Outline each blood parasite and name the species.
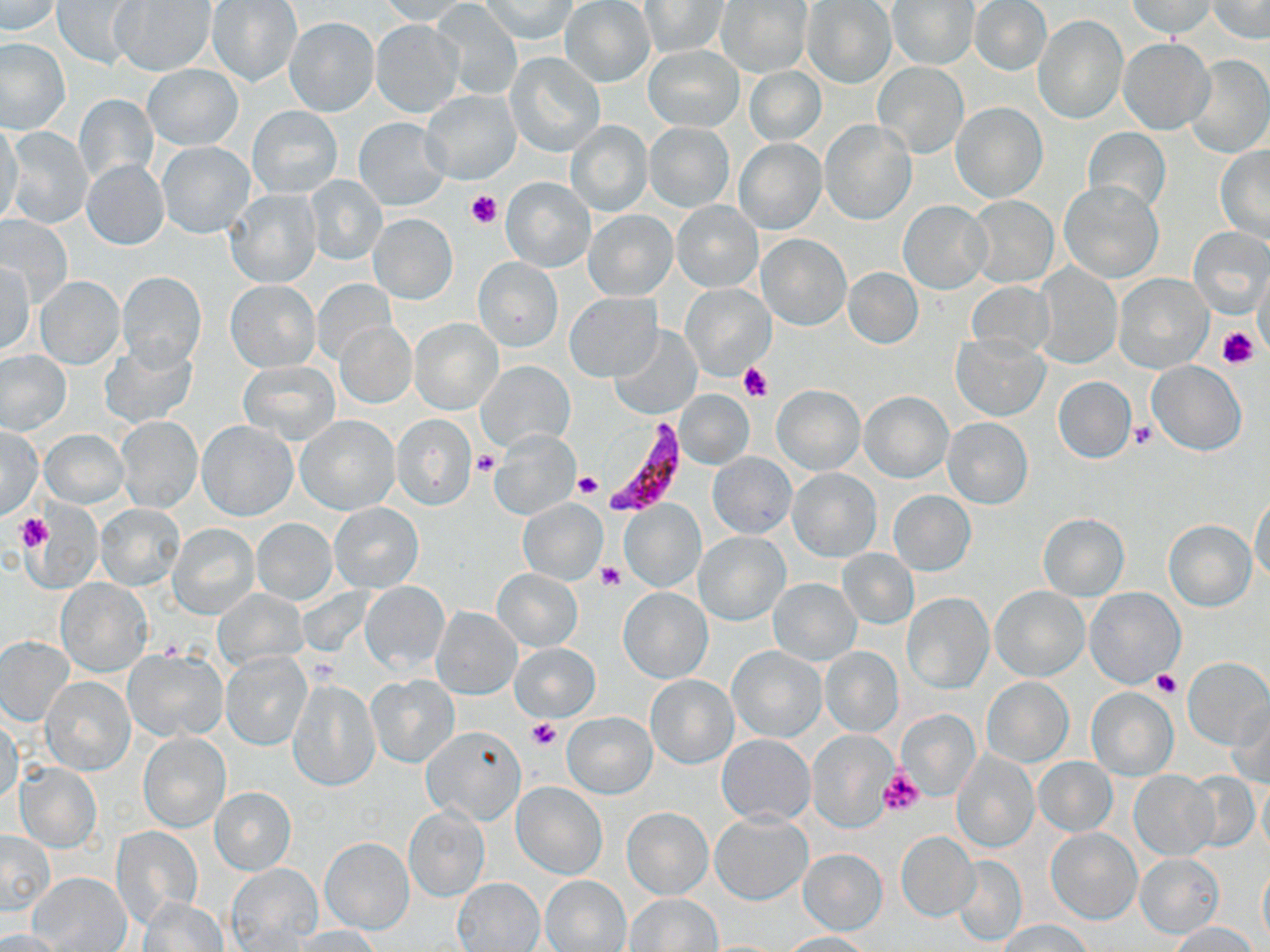

Approximate bounding boxes as named x1/y1/x2/y2 corners in pixels.
Plasmodium falciparum-infected red blood cells: (x1=599, y1=419, x2=692, y2=516).
No Plasmodium ovale, Plasmodium malariae, Plasmodium vivax, Babesia divergens, or Trypanosoma brucei observed.

Summary:
  - Uninfected red blood cell locations: (x1=53, y1=0, x2=140, y2=69), (x1=377, y1=0, x2=474, y2=26), (x1=560, y1=0, x2=655, y2=88), (x1=970, y1=0, x2=1051, y2=76), (x1=1129, y1=0, x2=1214, y2=38), (x1=1206, y1=0, x2=1270, y2=42), (x1=1, y1=1, x2=63, y2=35), (x1=110, y1=1, x2=216, y2=76), (x1=206, y1=1, x2=301, y2=86), (x1=481, y1=1, x2=577, y2=41), (x1=641, y1=1, x2=727, y2=57), (x1=890, y1=1, x2=977, y2=68), (x1=716, y1=2, x2=811, y2=78), (x1=802, y1=2, x2=895, y2=89), (x1=432, y1=4, x2=523, y2=98), (x1=1034, y1=15, x2=1127, y2=123), (x1=285, y1=16, x2=378, y2=117), (x1=370, y1=20, x2=464, y2=118), (x1=1, y1=38, x2=69, y2=133), (x1=1119, y1=38, x2=1213, y2=134), (x1=643, y1=45, x2=743, y2=132), (x1=506, y1=52, x2=604, y2=158), (x1=1186, y1=54, x2=1269, y2=157), (x1=873, y1=62, x2=969, y2=159), (x1=143, y1=64, x2=243, y2=150), (x1=744, y1=66, x2=825, y2=146), (x1=422, y1=89, x2=521, y2=184), (x1=73, y1=94, x2=158, y2=184), (x1=951, y1=103, x2=1048, y2=203), (x1=249, y1=105, x2=342, y2=198), (x1=353, y1=117, x2=449, y2=210), (x1=819, y1=119, x2=915, y2=223), (x1=564, y1=120, x2=652, y2=217), (x1=0, y1=121, x2=24, y2=226), (x1=644, y1=122, x2=734, y2=211), (x1=4, y1=127, x2=92, y2=229), (x1=1083, y1=127, x2=1171, y2=215), (x1=735, y1=139, x2=826, y2=234), (x1=158, y1=141, x2=255, y2=237), (x1=1215, y1=147, x2=1270, y2=242), (x1=82, y1=160, x2=168, y2=249), (x1=306, y1=176, x2=386, y2=263), (x1=500, y1=177, x2=596, y2=272), (x1=1059, y1=181, x2=1163, y2=283), (x1=225, y1=190, x2=320, y2=288), (x1=967, y1=196, x2=1058, y2=287), (x1=674, y1=199, x2=763, y2=293), (x1=899, y1=201, x2=990, y2=293), (x1=582, y1=209, x2=678, y2=301), (x1=368, y1=213, x2=457, y2=304), (x1=0, y1=215, x2=72, y2=307), (x1=1187, y1=227, x2=1269, y2=314), (x1=757, y1=234, x2=850, y2=330), (x1=472, y1=257, x2=563, y2=352), (x1=0, y1=259, x2=36, y2=354), (x1=1034, y1=263, x2=1122, y2=368), (x1=1254, y1=265, x2=1269, y2=360), (x1=844, y1=267, x2=923, y2=348), (x1=117, y1=272, x2=207, y2=369), (x1=1114, y1=273, x2=1212, y2=373), (x1=34, y1=275, x2=125, y2=369), (x1=226, y1=280, x2=319, y2=372), (x1=313, y1=280, x2=396, y2=365), (x1=965, y1=281, x2=1057, y2=358), (x1=682, y1=284, x2=774, y2=378), (x1=564, y1=292, x2=662, y2=381), (x1=409, y1=318, x2=502, y2=414), (x1=336, y1=320, x2=416, y2=408), (x1=610, y1=325, x2=703, y2=419), (x1=952, y1=335, x2=1048, y2=421), (x1=99, y1=341, x2=198, y2=428), (x1=1, y1=350, x2=71, y2=434), (x1=239, y1=360, x2=340, y2=444), (x1=478, y1=360, x2=575, y2=450), (x1=1147, y1=360, x2=1246, y2=455), (x1=1052, y1=375, x2=1136, y2=463), (x1=771, y1=385, x2=866, y2=475), (x1=676, y1=389, x2=753, y2=468), (x1=860, y1=390, x2=953, y2=483), (x1=295, y1=414, x2=399, y2=514), (x1=391, y1=414, x2=477, y2=510), (x1=115, y1=415, x2=202, y2=513), (x1=943, y1=417, x2=1033, y2=509), (x1=198, y1=420, x2=296, y2=521), (x1=1, y1=425, x2=40, y2=519), (x1=41, y1=428, x2=129, y2=507), (x1=489, y1=429, x2=580, y2=520), (x1=708, y1=453, x2=797, y2=538), (x1=787, y1=467, x2=881, y2=562), (x1=889, y1=491, x2=975, y2=575), (x1=1251, y1=491, x2=1270, y2=584), (x1=517, y1=498, x2=608, y2=585), (x1=620, y1=498, x2=706, y2=593), (x1=328, y1=501, x2=424, y2=592), (x1=96, y1=502, x2=187, y2=592), (x1=21, y1=506, x2=104, y2=593), (x1=1037, y1=514, x2=1129, y2=600), (x1=253, y1=518, x2=336, y2=605), (x1=1164, y1=519, x2=1256, y2=611), (x1=168, y1=524, x2=260, y2=620), (x1=695, y1=532, x2=788, y2=625), (x1=837, y1=548, x2=918, y2=629), (x1=492, y1=568, x2=582, y2=652), (x1=769, y1=578, x2=862, y2=666), (x1=57, y1=579, x2=150, y2=675), (x1=360, y1=581, x2=449, y2=674), (x1=990, y1=585, x2=1090, y2=681), (x1=618, y1=586, x2=712, y2=683), (x1=214, y1=589, x2=306, y2=668), (x1=1086, y1=589, x2=1187, y2=690), (x1=902, y1=593, x2=993, y2=693), (x1=431, y1=607, x2=522, y2=699), (x1=0, y1=637, x2=73, y2=725), (x1=511, y1=643, x2=600, y2=722), (x1=727, y1=645, x2=827, y2=742), (x1=821, y1=646, x2=902, y2=736), (x1=123, y1=650, x2=228, y2=742), (x1=222, y1=652, x2=310, y2=749), (x1=1182, y1=657, x2=1270, y2=749), (x1=365, y1=673, x2=460, y2=768), (x1=646, y1=674, x2=737, y2=768), (x1=41, y1=676, x2=135, y2=775), (x1=982, y1=676, x2=1073, y2=766), (x1=288, y1=677, x2=382, y2=791), (x1=1087, y1=687, x2=1178, y2=780), (x1=1229, y1=700, x2=1270, y2=787), (x1=897, y1=708, x2=981, y2=802), (x1=563, y1=711, x2=656, y2=798), (x1=0, y1=716, x2=22, y2=809), (x1=420, y1=725, x2=526, y2=824), (x1=805, y1=730, x2=897, y2=832), (x1=138, y1=732, x2=231, y2=832), (x1=718, y1=735, x2=814, y2=826), (x1=951, y1=750, x2=1038, y2=853), (x1=1034, y1=757, x2=1117, y2=836), (x1=15, y1=763, x2=102, y2=852), (x1=1129, y1=770, x2=1219, y2=860), (x1=1184, y1=771, x2=1261, y2=853), (x1=1257, y1=777, x2=1270, y2=859), (x1=513, y1=782, x2=606, y2=879), (x1=209, y1=786, x2=296, y2=875), (x1=622, y1=807, x2=713, y2=899), (x1=404, y1=808, x2=489, y2=901), (x1=712, y1=812, x2=812, y2=904), (x1=112, y1=826, x2=203, y2=925), (x1=1047, y1=828, x2=1141, y2=924), (x1=1, y1=830, x2=54, y2=914), (x1=897, y1=831, x2=979, y2=921), (x1=321, y1=837, x2=414, y2=934), (x1=799, y1=849, x2=887, y2=934), (x1=1135, y1=853, x2=1223, y2=937), (x1=951, y1=854, x2=1027, y2=945), (x1=227, y1=863, x2=322, y2=950), (x1=1258, y1=863, x2=1270, y2=946), (x1=31, y1=872, x2=131, y2=952), (x1=540, y1=874, x2=631, y2=952), (x1=454, y1=878, x2=545, y2=950), (x1=625, y1=893, x2=722, y2=951), (x1=139, y1=899, x2=227, y2=952), (x1=1000, y1=919, x2=1091, y2=952), (x1=1170, y1=921, x2=1260, y2=951), (x1=292, y1=926, x2=384, y2=951), (x1=0, y1=928, x2=69, y2=952), (x1=780, y1=932, x2=874, y2=952)
  - Platelet locations: (x1=467, y1=190, x2=503, y2=228), (x1=1217, y1=326, x2=1258, y2=367), (x1=740, y1=362, x2=772, y2=400), (x1=1130, y1=421, x2=1157, y2=449), (x1=474, y1=451, x2=501, y2=477), (x1=571, y1=473, x2=601, y2=498), (x1=16, y1=512, x2=71, y2=570), (x1=17, y1=514, x2=52, y2=552), (x1=597, y1=561, x2=626, y2=591), (x1=158, y1=640, x2=184, y2=659), (x1=304, y1=653, x2=341, y2=686), (x1=1153, y1=672, x2=1181, y2=697), (x1=526, y1=718, x2=561, y2=751), (x1=878, y1=770, x2=924, y2=816)
  - Slide-level diagnosis: Plasmodium falciparum
  - Preparation: thin blood smear
  - Magnification: 1000x
  - Field of view: one of a larger specimen
  - Stain: May-Grünwald-Giemsa
  - Image size: 1270×952 pixels
  - Modality: light microscopy